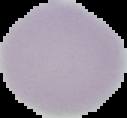
image type = segmented cell region with the area outside set to black
preparation = thin blood film
image size = 127×118 pixels
malaria status = uninfected